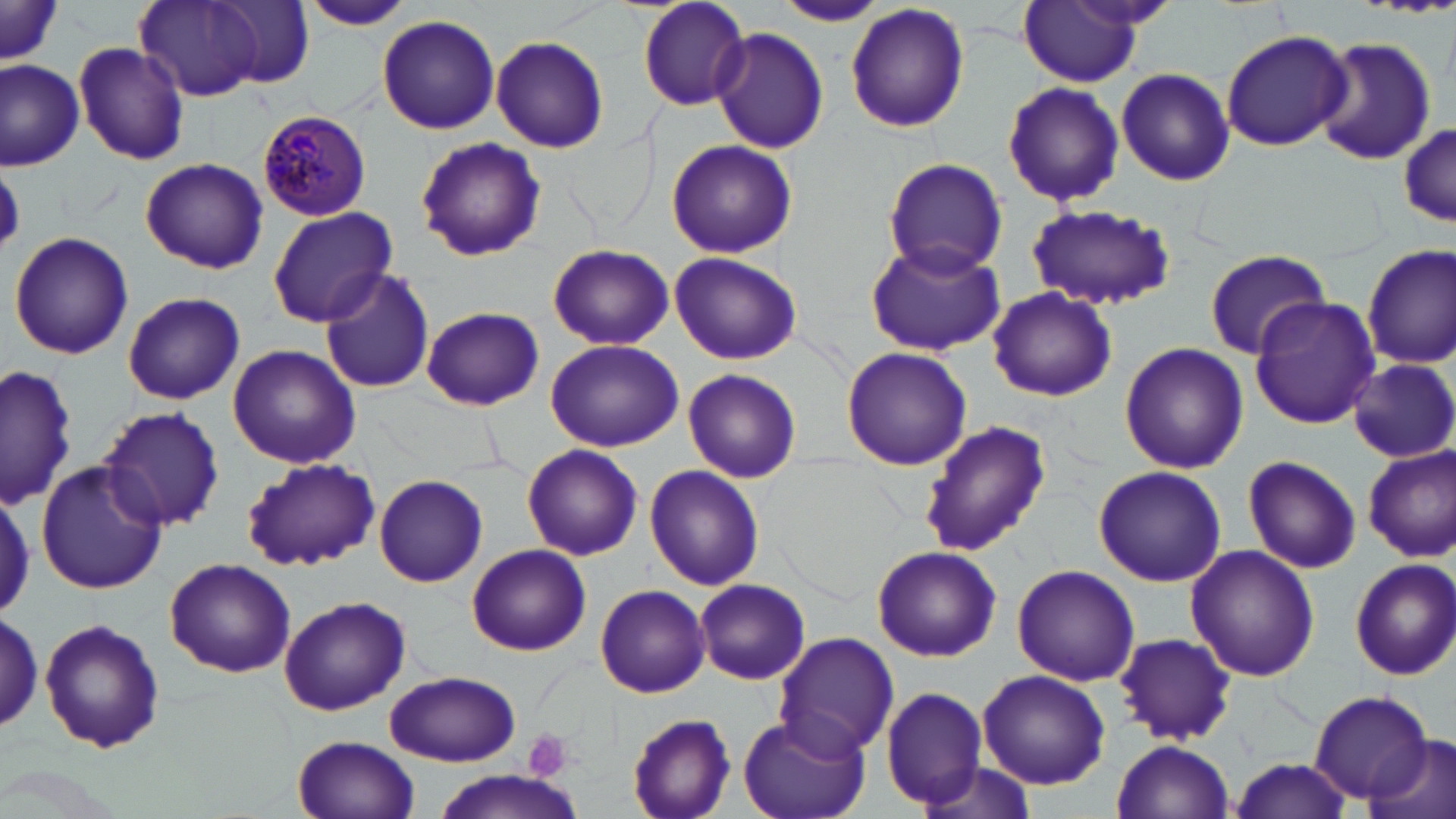
slide_level_diagnosis: Plasmodium malariae
magnification: 1000x
uninfected_red_blood_cell_locations: 'approximate bounding boxes as [x1, y1, x2, y2] in pixels: [133, 0, 262, 103], [634, 0, 751, 112], [211, 1, 315, 88], [294, 1, 417, 30], [776, 1, 885, 27], [1016, 1, 1147, 85], [844, 2, 971, 135], [0, 3, 64, 71], [376, 14, 501, 134], [709, 27, 829, 154], [1221, 28, 1354, 152], [490, 35, 609, 153], [1312, 36, 1436, 168], [73, 41, 191, 166], [1, 60, 84, 168], [1114, 67, 1236, 186], [1002, 81, 1125, 208], [1396, 120, 1453, 230], [414, 138, 545, 260], [665, 139, 799, 259], [883, 156, 1008, 278], [140, 158, 267, 274], [1025, 203, 1177, 311], [266, 206, 398, 326], [8, 232, 134, 360], [548, 242, 674, 348], [864, 242, 1005, 357], [1362, 243, 1456, 370], [1203, 248, 1331, 358], [669, 252, 802, 366], [318, 268, 436, 394], [987, 285, 1118, 403], [121, 291, 245, 405], [1249, 297, 1382, 430], [421, 306, 543, 412], [544, 339, 684, 453], [1119, 343, 1248, 474], [227, 344, 362, 469], [840, 346, 972, 470], [1348, 359, 1454, 462], [0, 363, 80, 511], [683, 367, 801, 481], [100, 405, 226, 534], [917, 419, 1051, 556], [1363, 443, 1456, 562], [522, 444, 644, 561], [1241, 455, 1361, 573], [35, 459, 167, 597], [241, 459, 379, 572], [1094, 465, 1226, 586], [644, 466, 763, 589], [374, 474, 488, 587], [0, 485, 34, 623], [466, 543, 591, 655], [1185, 544, 1320, 685], [872, 545, 1001, 661], [164, 558, 295, 679], [1348, 558, 1456, 680], [1011, 564, 1140, 686], [696, 579, 813, 686], [595, 584, 711, 699], [278, 596, 409, 717], [0, 609, 48, 738], [39, 617, 166, 755], [773, 632, 900, 758], [1114, 632, 1237, 746], [977, 668, 1111, 790], [385, 671, 521, 766], [880, 686, 990, 810], [1310, 691, 1440, 804], [735, 711, 872, 819], [626, 713, 737, 819], [294, 734, 419, 819], [1368, 734, 1456, 819], [1112, 739, 1234, 819], [911, 756, 1042, 819], [1230, 756, 1356, 819], [426, 771, 586, 819]'
stain: May-Grünwald-Giemsa
modality: optical microscopy
field_of_view: one of a larger specimen
platelet_locations: 'approximate bounding boxes as [x1, y1, x2, y2] in pixels: [522, 729, 574, 782]'
plasmodium_malariae_infected_red_blood_cell_locations: 'approximate bounding boxes as [x1, y1, x2, y2] in pixels: [257, 110, 372, 219]'
preparation: thin blood film
image_size: 1456×819 pixels